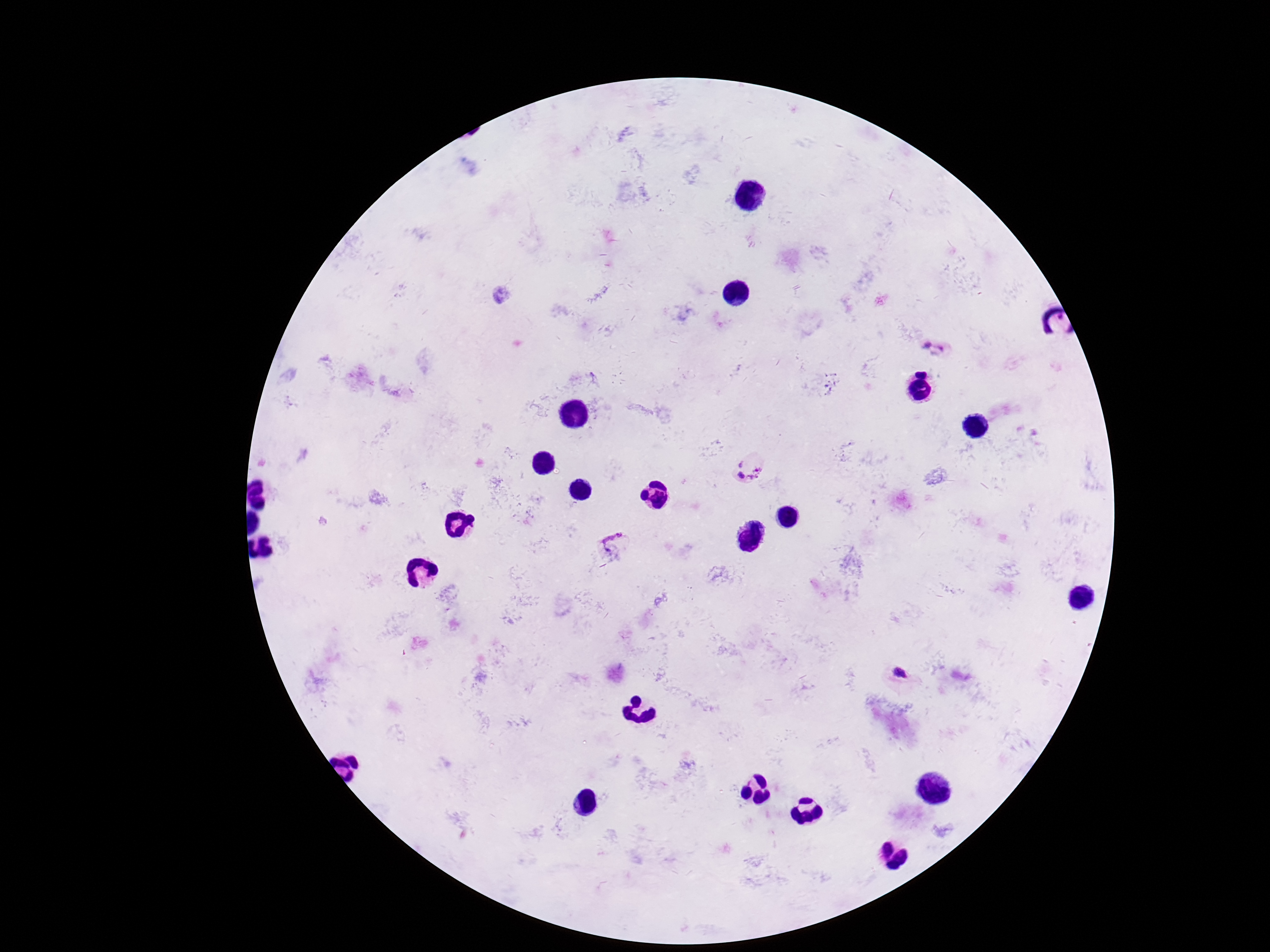
Approximate centers as {x, y} in pixels.
Summary:
  - Plasmodium parasite locations: {936, 347}, {749, 465}, {614, 545}, {900, 673}
  - Stain: Giemsa
  - Magnification: 100x
  - Capture: smartphone camera through the microscope eyepiece
  - Patient malaria status: infected
  - Field of view: single
  - Image size: 1270×952 pixels
  - Preparation: thick peripheral-blood smear